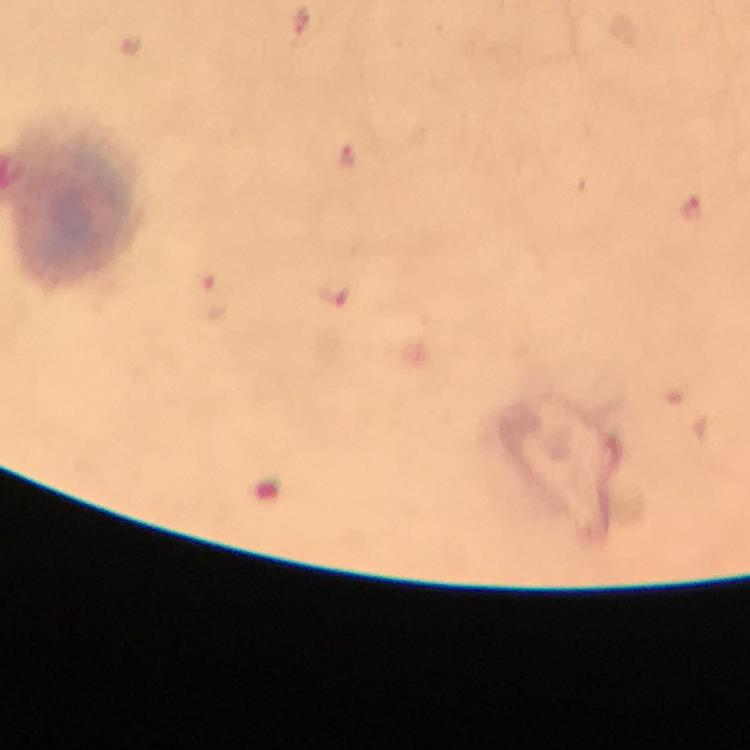
Approximate object centers, in pixels from the top-left corner. Plasmodium parasite locations: (x=348, y=155), (x=691, y=209), (x=336, y=291), (x=216, y=297). From a malaria diagnostic workup. Smartphone photograph taken through a microscope. Thick blood smear. Image is 750×750 pixels. Immersion oil applied. At 100x magnification. Giemsa stain. Cropped region of a single field of view.